Identify the parasite.
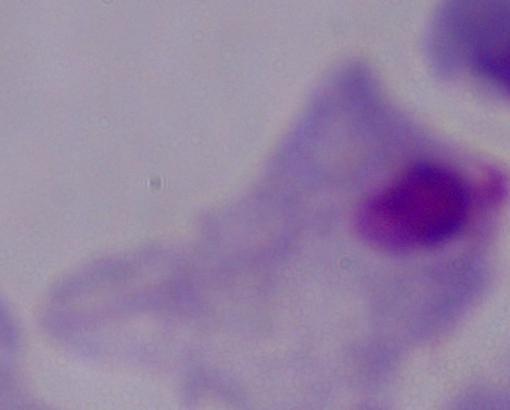
A trichomonad.

{
  "magnification": "1000x",
  "modality": "photomicrograph"
}